Assess this cell for malaria.
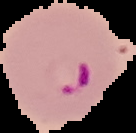

It is parasitized.

Image is 136×133 pixels. The area outside the segmented cell region is set to black. From a thin blood film.